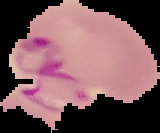

Image is 160×133 pixels. Cell region segmented out of the field of view; the surrounding area is masked to black. Result: Plasmodium parasites identified. From a thin blood film.